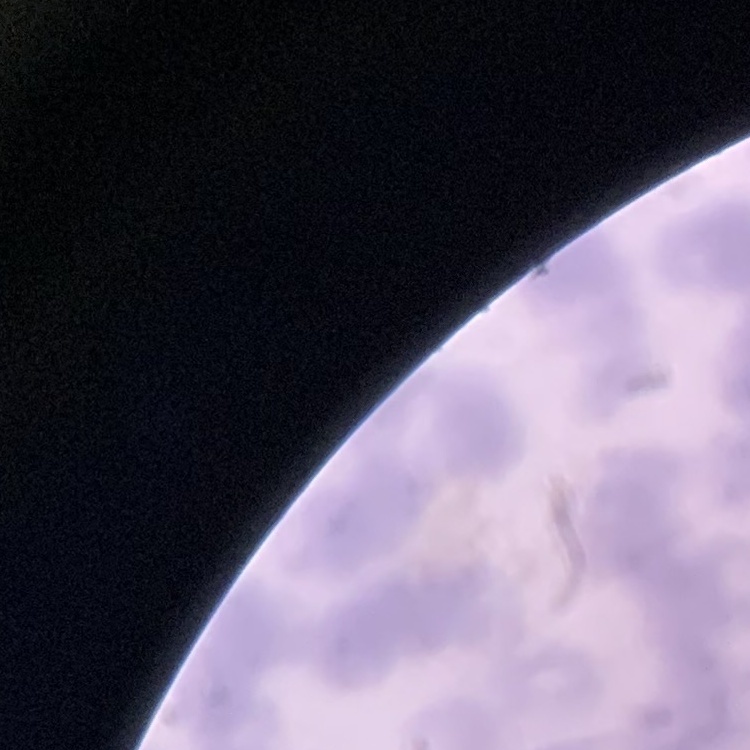

erythrocyte_morphology: rouleaux formation
stain: Field's or Giemsa
preparation: thin blood smear
image_type: square crop of a larger photomicrograph